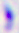

Summary:
  - Magnification: 400x
  - Identification: Toxoplasma gondii
  - Modality: micrograph